Give the preparation type.
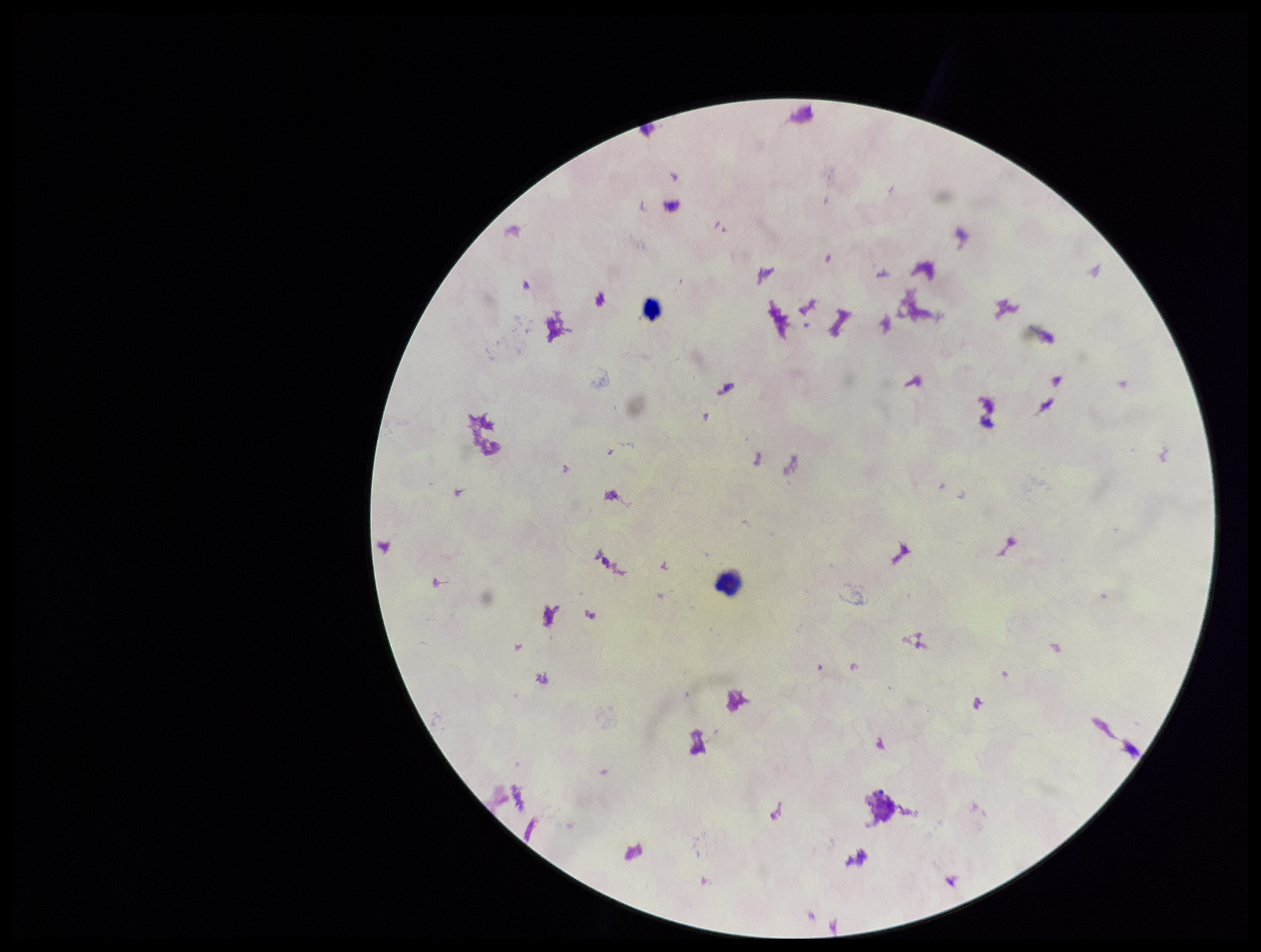
It is a thick blood smear.

Giemsa stain. Parasite count: 0. Patient malaria status: negative. Leukocyte count: 2. Smartphone photograph taken through the eyepiece of a microscope. Plasmodium parasites: none identified. Image is 1261×952 pixels. One field from this slide.